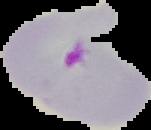 Result: Plasmodium parasites identified. Segmented cell region on a black background. From a thin blood film. Image is 151×130 pixels.